State the blood parasite species.
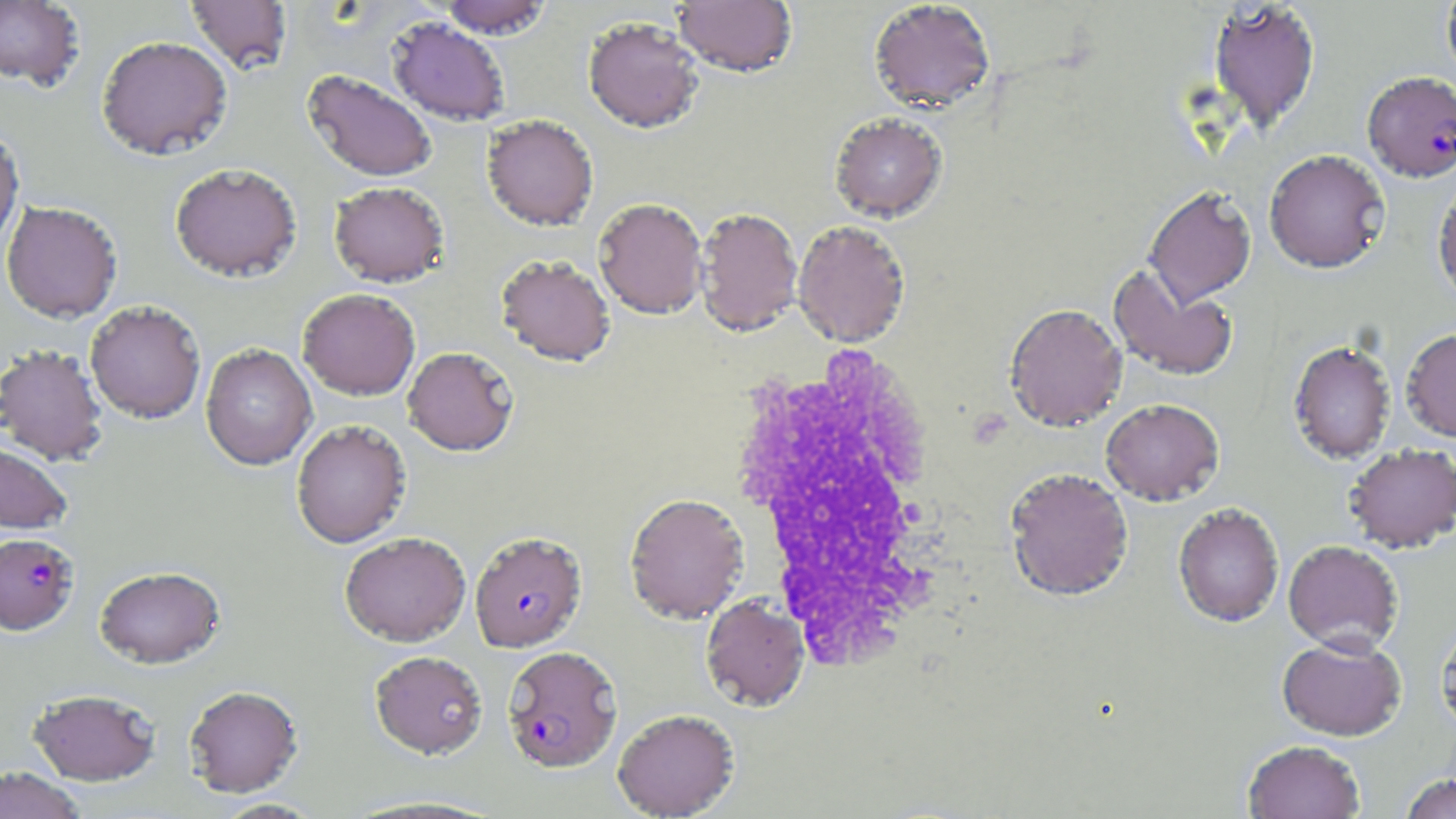

Plasmodium falciparum.

Approximate bounding boxes as (x1,y1)-(x2,y2) corner pairs in pixels. White blood cell locations: (722,343)-(960,669). Plasmodium falciparum-infected red blood cell locations: (1362,71)-(1456,182), (470,531)-(587,653), (0,532)-(79,635), (502,645)-(622,773). Uninfected red blood cell locations: (0,0)-(86,91), (185,0)-(292,75), (437,0)-(554,38), (1442,0)-(1456,83), (672,1)-(798,78), (868,1)-(996,114), (1208,1)-(1321,133), (583,16)-(705,133), (388,17)-(510,126), (96,35)-(232,160), (302,70)-(437,182), (829,113)-(947,223), (481,115)-(599,232), (0,124)-(24,255), (1263,149)-(1390,273), (169,163)-(302,282), (1432,175)-(1456,306), (329,181)-(449,287), (1143,185)-(1256,306), (593,198)-(708,319), (1,200)-(123,323), (695,207)-(803,337), (792,220)-(911,347), (495,254)-(616,367), (1108,263)-(1239,382), (297,288)-(420,400), (84,300)-(206,423), (1004,302)-(1127,432), (1401,328)-(1456,441), (1288,339)-(1397,463), (201,343)-(316,470), (0,344)-(108,465), (402,346)-(519,456), (1101,398)-(1224,505), (291,419)-(411,548), (0,440)-(73,533), (1344,443)-(1456,553), (1004,467)-(1134,602), (624,492)-(749,624), (1173,503)-(1285,628), (339,531)-(471,646), (1283,540)-(1403,653), (94,565)-(226,669), (701,595)-(809,711), (1435,618)-(1456,737), (1277,635)-(1407,741), (370,650)-(487,758), (184,684)-(304,797), (28,688)-(161,785), (612,708)-(740,818), (1242,740)-(1365,819), (0,766)-(87,819), (1398,772)-(1456,818), (212,798)-(324,818). Thin blood film. Single field of view. May-Grünwald-Giemsa-stained preparation. Light microscopy. 1000x magnification. Image is 1456×819 pixels.